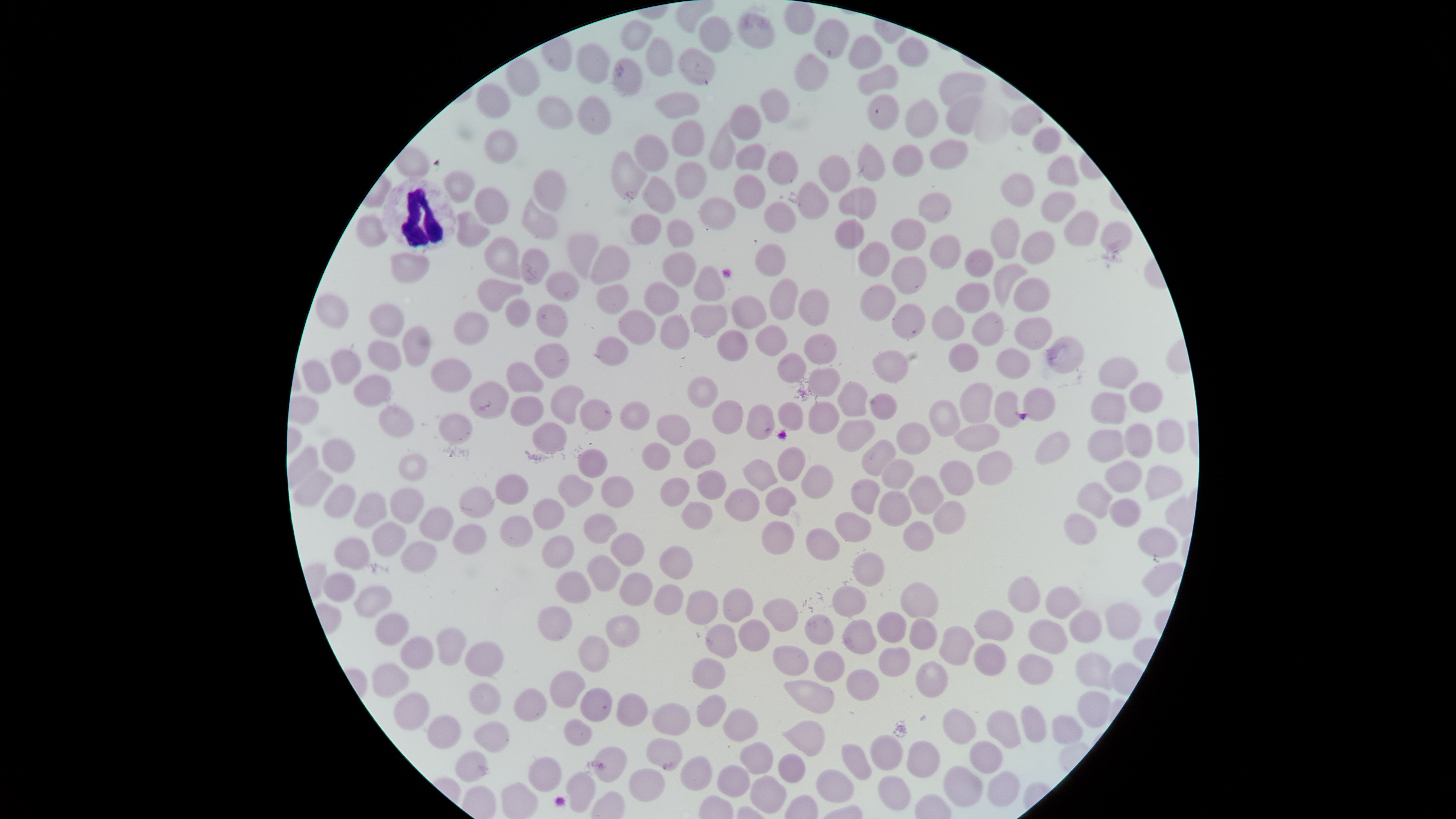
presence: no malaria parasites identified
image_size: 1456×819 pixels
field_of_view: single
uninfected_red_blood_cells: 'approximate bounding boxes as (left, top, right, bottom) in pixels: (784, 3, 815, 35), (737, 13, 776, 49), (699, 16, 731, 53), (815, 18, 849, 59), (621, 19, 653, 51), (849, 34, 882, 70), (645, 37, 672, 77), (897, 37, 929, 68), (576, 43, 610, 84), (677, 47, 716, 86), (794, 53, 829, 92), (505, 58, 540, 97), (611, 58, 642, 96), (858, 65, 899, 96), (939, 73, 988, 105), (475, 83, 511, 119), (760, 88, 791, 124), (654, 92, 700, 120), (867, 94, 899, 130), (577, 96, 611, 134), (946, 96, 981, 136), (537, 97, 574, 130), (906, 99, 939, 138), (730, 106, 761, 141), (1010, 106, 1044, 137), (672, 120, 704, 157), (708, 123, 736, 171), (1033, 127, 1062, 155), (484, 129, 518, 165), (633, 134, 669, 173), (930, 139, 968, 170), (858, 143, 885, 182), (735, 144, 765, 170), (892, 144, 924, 178), (610, 151, 648, 201), (767, 151, 799, 186), (819, 155, 852, 193), (1048, 155, 1079, 187), (674, 162, 708, 199), (532, 169, 567, 211), (444, 171, 476, 203), (1000, 173, 1035, 207), (734, 175, 766, 209), (642, 177, 676, 214), (797, 181, 830, 220), (474, 187, 509, 225), (838, 187, 877, 220), (919, 192, 952, 223), (1042, 192, 1075, 222), (521, 197, 558, 240), (699, 197, 736, 230), (764, 202, 796, 234), (457, 211, 490, 248), (1063, 211, 1098, 247), (629, 214, 662, 244), (355, 215, 388, 248), (835, 218, 864, 249), (891, 218, 927, 251), (991, 218, 1020, 259), (666, 219, 696, 248), (1100, 222, 1132, 253), (1021, 231, 1055, 265), (567, 234, 599, 279), (929, 235, 961, 269), (483, 237, 521, 279), (858, 241, 890, 277), (754, 243, 786, 277), (589, 245, 630, 285), (520, 248, 550, 286), (965, 249, 994, 277), (661, 251, 697, 287), (390, 252, 430, 284), (891, 256, 927, 295), (993, 264, 1028, 308), (693, 266, 725, 301), (545, 271, 579, 302), (476, 278, 524, 312), (769, 278, 799, 321), (1014, 278, 1051, 313), (643, 282, 679, 316), (596, 283, 630, 315), (955, 283, 990, 313), (860, 285, 897, 321), (797, 288, 830, 326), (315, 294, 349, 329), (731, 296, 767, 330), (504, 298, 531, 328), (369, 303, 405, 338), (892, 303, 926, 339), (535, 304, 569, 338), (689, 304, 728, 337), (932, 305, 965, 341), (618, 309, 656, 345), (452, 311, 489, 346), (973, 311, 1004, 346), (660, 314, 690, 350), (1014, 316, 1053, 350), (754, 324, 788, 357), (401, 325, 431, 367), (716, 329, 749, 362), (803, 332, 837, 365), (596, 336, 629, 367), (1046, 337, 1084, 374), (366, 340, 402, 372), (948, 342, 979, 373), (534, 343, 570, 379), (330, 349, 362, 385), (996, 349, 1031, 379), (872, 350, 909, 383), (777, 352, 808, 384), (1098, 357, 1138, 390), (430, 358, 472, 393), (301, 359, 332, 394), (506, 362, 544, 393), (808, 367, 841, 397), (353, 374, 391, 407), (686, 376, 718, 408), (469, 381, 510, 418), (837, 381, 868, 417), (1128, 381, 1163, 413), (959, 382, 993, 423), (550, 385, 585, 425), (1023, 387, 1055, 422), (994, 390, 1020, 428), (869, 392, 898, 420), (1090, 392, 1126, 425), (510, 396, 544, 427), (579, 398, 612, 432), (711, 399, 743, 435), (929, 399, 961, 437), (619, 401, 650, 431), (808, 401, 840, 435), (777, 402, 804, 431), (745, 404, 775, 440), (378, 405, 415, 438), (438, 413, 473, 445), (657, 414, 691, 446), (1155, 418, 1185, 454), (837, 419, 875, 452), (532, 422, 567, 454), (895, 422, 932, 455), (953, 423, 1001, 452), (1124, 423, 1153, 459), (1087, 429, 1124, 463), (1035, 431, 1071, 465), (321, 438, 355, 474), (683, 438, 716, 469), (861, 439, 897, 476), (642, 442, 671, 472), (776, 446, 806, 481), (577, 448, 607, 479), (976, 450, 1012, 486), (397, 454, 428, 482), (880, 458, 915, 489), (742, 459, 778, 491), (939, 460, 974, 497), (1104, 460, 1142, 493), (800, 464, 834, 499), (1145, 466, 1183, 501), (292, 469, 334, 506), (696, 470, 726, 500), (557, 473, 594, 507), (494, 474, 528, 506), (907, 475, 945, 515), (600, 476, 634, 508), (659, 477, 690, 507), (851, 479, 880, 514), (1077, 482, 1112, 519), (322, 484, 356, 519), (764, 486, 797, 517), (390, 487, 425, 523), (459, 487, 494, 519), (724, 488, 760, 522), (878, 490, 912, 527), (353, 492, 388, 528), (531, 498, 565, 531), (1109, 498, 1141, 528), (932, 500, 966, 535), (680, 501, 713, 530), (419, 507, 454, 541), (834, 511, 872, 543), (582, 513, 617, 545), (1063, 513, 1097, 546), (499, 515, 534, 548), (760, 520, 794, 555), (902, 520, 934, 552), (371, 521, 407, 558), (452, 523, 486, 556), (1137, 527, 1178, 558), (805, 528, 840, 562), (610, 532, 645, 567), (541, 534, 574, 569), (333, 537, 370, 571), (400, 540, 437, 573), (659, 546, 693, 580), (852, 552, 885, 587), (586, 555, 621, 593), (1141, 562, 1183, 598), (555, 570, 591, 604), (619, 572, 653, 606), (322, 573, 356, 602), (1007, 576, 1041, 613), (900, 581, 939, 618), (653, 584, 684, 616), (831, 585, 867, 617), (353, 586, 392, 618), (1044, 586, 1081, 619), (722, 587, 754, 623), (685, 589, 718, 625), (762, 598, 799, 632), (1104, 602, 1141, 641), (537, 606, 573, 642), (973, 610, 1015, 641), (1068, 610, 1101, 644), (876, 611, 907, 643), (374, 612, 409, 646), (803, 613, 834, 645), (605, 614, 640, 648), (909, 618, 937, 650), (737, 619, 771, 652), (842, 619, 877, 655), (1027, 619, 1069, 655), (704, 623, 738, 659), (937, 625, 973, 666), (436, 628, 467, 666), (400, 636, 434, 670), (578, 636, 610, 673), (464, 641, 504, 677), (973, 642, 1007, 677), (772, 645, 809, 676), (878, 646, 911, 677), (813, 650, 845, 682), (1075, 652, 1112, 690), (1017, 653, 1053, 685), (692, 658, 726, 690), (915, 661, 949, 698), (371, 663, 409, 698), (845, 669, 880, 701), (549, 670, 586, 709), (783, 679, 836, 714), (468, 683, 501, 716), (514, 687, 548, 722), (579, 687, 613, 722), (1077, 691, 1112, 728), (393, 692, 430, 731), (616, 693, 648, 727), (696, 694, 727, 728), (652, 703, 691, 735), (1021, 705, 1047, 743), (722, 708, 759, 742), (942, 708, 977, 745), (986, 711, 1021, 749), (1052, 715, 1084, 745), (426, 716, 461, 749), (563, 718, 592, 746), (782, 720, 825, 757), (474, 722, 510, 753), (870, 735, 903, 771), (646, 738, 683, 771), (906, 740, 940, 778), (968, 740, 1003, 774), (740, 742, 774, 775), (840, 743, 873, 780), (593, 747, 627, 783), (455, 751, 487, 783), (777, 753, 806, 783), (680, 755, 713, 792), (527, 757, 562, 792), (716, 764, 751, 797), (943, 765, 983, 807), (629, 768, 664, 803), (816, 769, 855, 804), (987, 771, 1021, 807), (566, 772, 596, 813), (749, 775, 787, 814), (877, 775, 912, 811)'
stain: Giemsa
capture: smartphone photograph through the microscope eyepiece
preparation: thin blood film
white_blood_cells: 'approximate bounding boxes as (left, top, right, bottom) in pixels: (381, 176, 457, 255)'
visible_region: circular